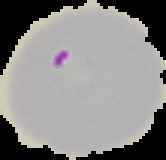 Cell region segmented out of the field of view; the surrounding area is masked to black. Malaria status: parasitized. From a thin blood smear. Image is 166×160 pixels.